Name the blood parasite species.
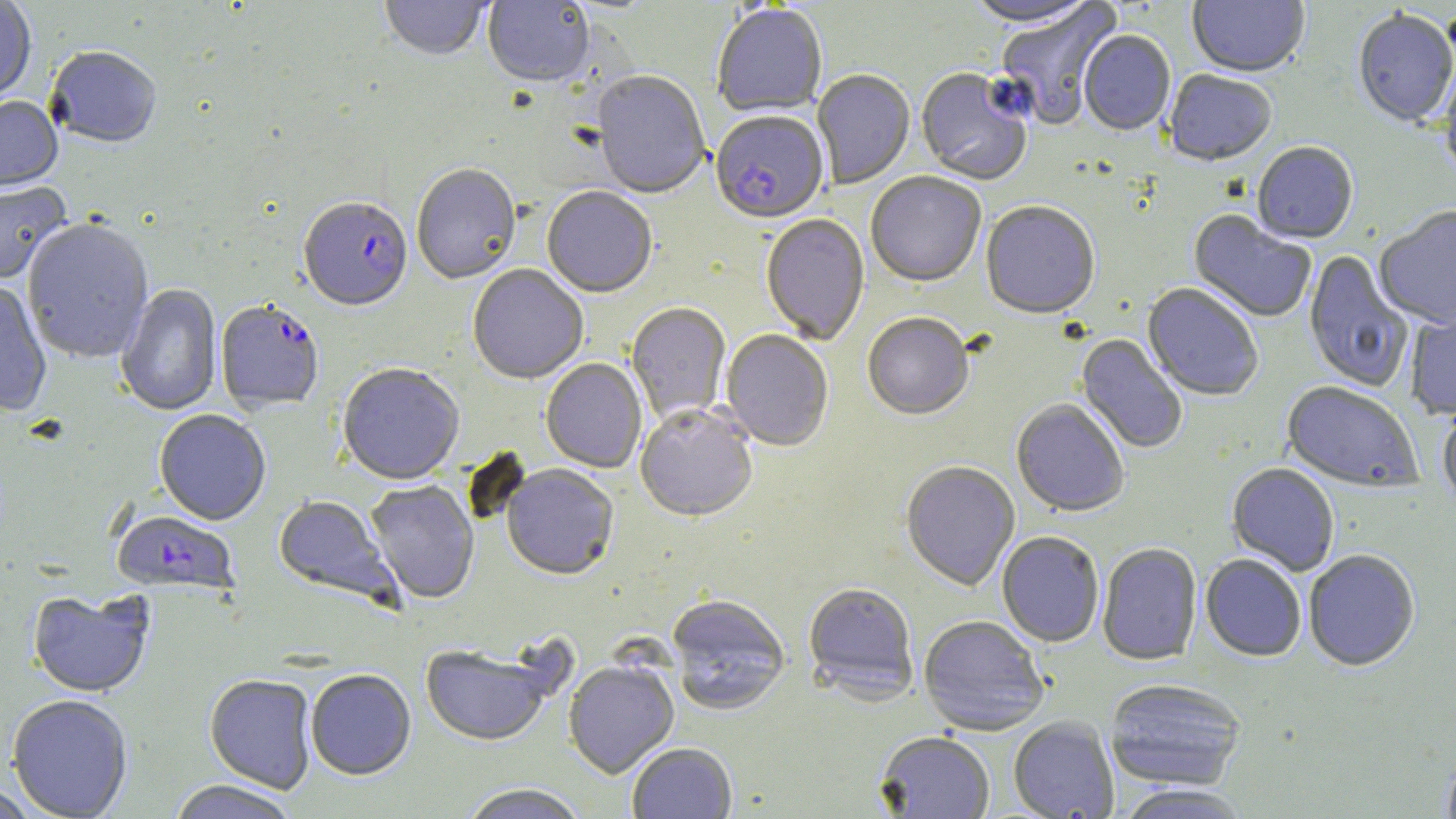

Plasmodium falciparum.

{
  "image_size": "1456×819 pixels",
  "modality": "optical microscopy",
  "preparation": "thin blood smear",
  "field_of_view": "one of a larger specimen",
  "plasmodium_falciparum_infected_red_blood_cell_locations": "approximate bounding boxes as [x1, y1, x2, y2] in pixels: [710, 112, 828, 226], [298, 200, 412, 314], [215, 302, 324, 414], [112, 511, 238, 598]",
  "uninfected_red_blood_cell_locations": "approximate bounding boxes as [x1, y1, x2, y2] in pixels: [379, 0, 490, 63], [962, 0, 1101, 29], [1187, 0, 1310, 80], [0, 1, 36, 105], [483, 1, 594, 88], [995, 3, 1123, 130], [712, 5, 828, 118], [1353, 12, 1456, 129], [1078, 32, 1175, 137], [46, 48, 161, 150], [1439, 66, 1456, 183], [812, 70, 915, 190], [915, 70, 1032, 187], [1163, 71, 1277, 168], [591, 72, 710, 201], [0, 98, 63, 194], [1252, 144, 1358, 246], [412, 165, 521, 286], [866, 173, 986, 289], [0, 182, 72, 286], [542, 188, 657, 299], [981, 203, 1100, 322], [1374, 208, 1456, 331], [1187, 211, 1316, 324], [760, 215, 870, 346], [22, 220, 154, 365], [1304, 251, 1413, 393], [467, 265, 588, 385], [0, 283, 52, 417], [116, 284, 223, 417], [1141, 284, 1263, 401], [626, 304, 731, 424], [1405, 305, 1456, 421], [862, 315, 974, 422], [720, 331, 834, 452], [1075, 333, 1187, 454], [541, 359, 647, 474], [337, 365, 464, 488], [1281, 383, 1423, 494], [1011, 400, 1129, 518], [635, 406, 758, 524], [1437, 406, 1456, 517], [154, 411, 271, 526], [901, 462, 1020, 592], [1226, 464, 1339, 577], [501, 466, 619, 582], [365, 481, 481, 605], [273, 495, 401, 608], [997, 532, 1104, 648], [1097, 543, 1202, 667], [1304, 551, 1420, 672], [1200, 554, 1306, 663], [803, 583, 918, 704], [27, 591, 154, 699], [668, 596, 790, 716], [919, 617, 1048, 736], [420, 646, 555, 748], [564, 662, 679, 780], [306, 671, 416, 782], [204, 674, 317, 794], [1104, 680, 1246, 791], [7, 695, 133, 819], [1008, 717, 1118, 819], [874, 733, 994, 818], [627, 744, 737, 819], [1441, 751, 1456, 819], [167, 781, 301, 819], [0, 783, 38, 819], [1113, 784, 1253, 819], [458, 785, 587, 819]",
  "magnification": "1000x",
  "stain": "May-Grünwald-Giemsa"
}